Report the malaria status of this cell.
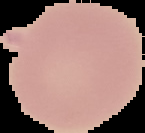
It is uninfected.

From a thin blood smear. Image is 145×133 pixels. Segmented cell region on a black background.